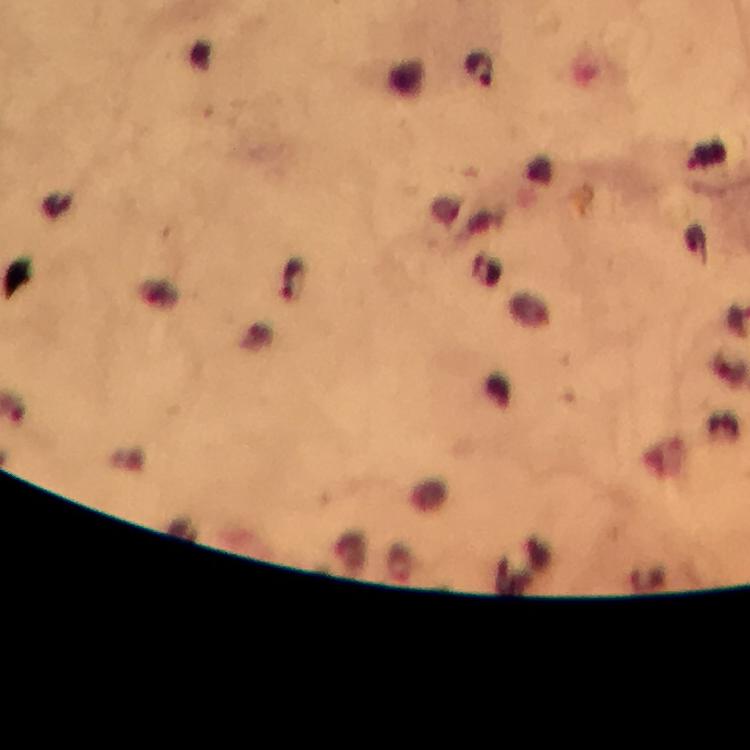

Approximate centers as [x, y] in pixels.
Summary:
  - Plasmodium parasite locations: [481, 69], [292, 283]
  - Magnification: 100x
  - Capture: smartphone mounted on the microscope
  - Stain: Giemsa
  - Context: from a malaria diagnostic workup
  - Image size: 750×750 pixels
  - Preparation: thick blood film
  - Cropped from: a single field of view
  - Immersion oil: used